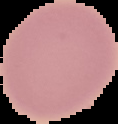

Malaria status: uninfected. Image is 118×124 pixels. Segmented cell region on a black background. From a thin blood film.